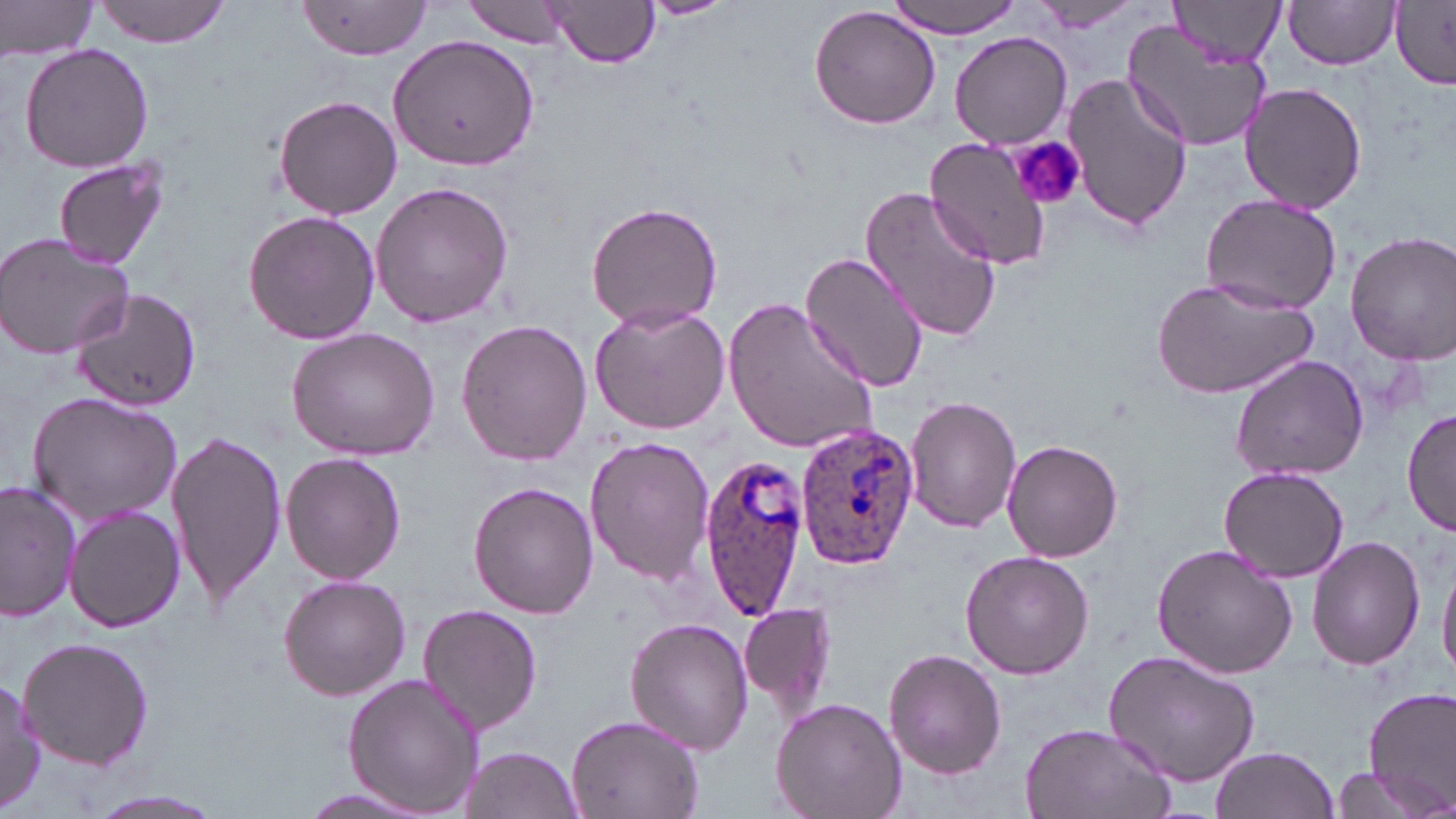

Summary:
  - Coordinate format: approximate bounding boxes as (x1, y1, x2, y2) in pixels
  - Platelet locations: (1008, 135, 1087, 213)
  - Uninfected red blood cell locations: (0, 0, 100, 60), (94, 0, 230, 46), (638, 0, 735, 19), (893, 0, 1022, 37), (1027, 0, 1143, 33), (1172, 0, 1285, 68), (1389, 0, 1456, 87), (462, 1, 572, 48), (1282, 1, 1401, 71), (296, 2, 433, 59), (545, 2, 659, 69), (809, 7, 940, 130), (1122, 20, 1270, 154), (389, 30, 540, 172), (950, 32, 1072, 148), (19, 42, 155, 174), (1063, 74, 1192, 233), (1238, 80, 1366, 214), (272, 93, 403, 220), (924, 136, 1054, 270), (53, 157, 170, 271), (370, 180, 516, 329), (861, 185, 1002, 344), (1198, 192, 1344, 314), (586, 200, 724, 332), (243, 208, 380, 347), (1346, 231, 1456, 363), (0, 232, 135, 360), (799, 248, 930, 394), (1150, 277, 1318, 402), (69, 289, 202, 409), (725, 295, 881, 458), (589, 300, 733, 436), (454, 318, 592, 464), (285, 326, 443, 461), (1230, 353, 1371, 483), (26, 390, 183, 526), (905, 395, 1022, 534), (1403, 408, 1456, 541), (166, 426, 287, 611), (583, 434, 714, 588), (1001, 440, 1123, 562), (281, 452, 406, 585), (1218, 466, 1350, 583), (0, 481, 79, 622), (469, 481, 599, 619), (1174, 486, 1323, 645), (66, 504, 185, 633), (1309, 534, 1426, 670), (1152, 542, 1299, 679), (959, 550, 1095, 679), (1438, 553, 1456, 684), (276, 573, 411, 702), (740, 600, 837, 716), (416, 603, 544, 734), (626, 617, 753, 756), (16, 635, 155, 770), (884, 648, 1006, 778), (1103, 650, 1261, 787), (342, 675, 486, 815), (0, 677, 45, 815), (1363, 689, 1456, 811), (771, 697, 907, 819), (566, 712, 705, 819), (1020, 721, 1175, 819), (1210, 746, 1340, 819), (459, 747, 584, 817), (1325, 765, 1439, 819), (76, 787, 232, 819), (294, 787, 434, 816)
  - Plasmodium ovale-infected red blood cell locations: (795, 424, 918, 569), (698, 452, 812, 618)
  - Slide-level diagnosis: Plasmodium ovale
  - Stain: May-Grünwald-Giemsa
  - Image size: 1456×819 pixels
  - Field of view: single
  - Preparation: thin blood smear
  - Magnification: 1000x
  - Modality: optical microscopy